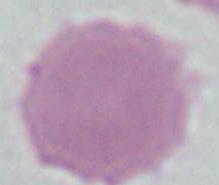

Summary:
  - Modality: micrograph
  - Identification: red blood cell
  - Magnification: 1000x